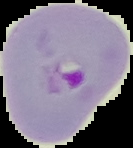
malaria_status: parasitized
preparation: thin blood film
image_type: cell region segmented out of the field of view; surrounding area masked to black
image_size: 133×148 pixels